Identify the cell.
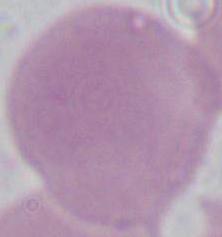

An erythrocyte.

Summary:
  - Magnification: 1000x
  - Modality: micrograph